Assess the morphology of the red blood cells.
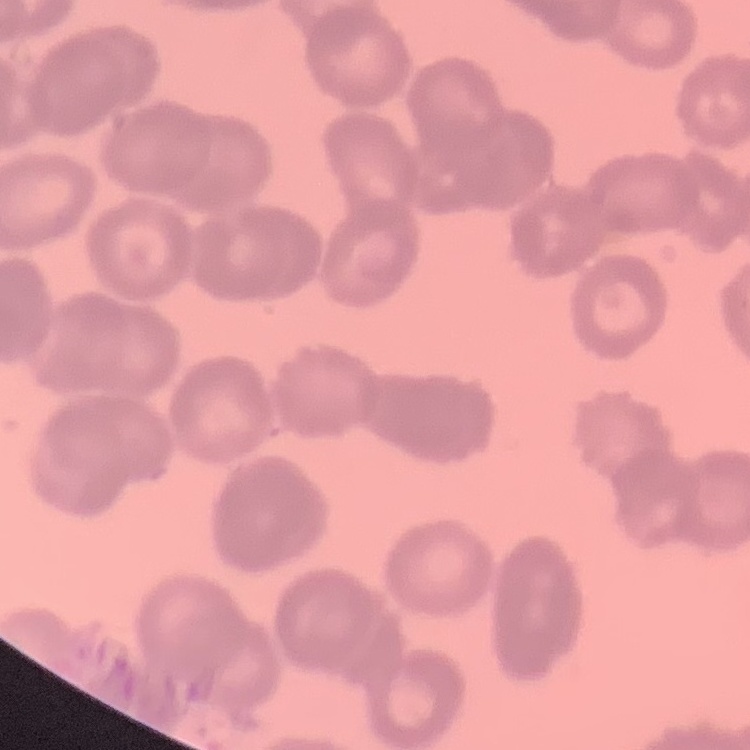

They show rouleaux formation.

Summary:
  - Stain: Field's or Giemsa
  - Image type: square crop of a larger photomicrograph
  - Preparation: thin blood smear